Classify this cell by malaria status.
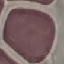

Uninfected.

stain = Giemsa
image type = automatically extracted cell patch, resized to 64 × 64 pixels
capture = smartphone through the microscope eyepiece
preparation = thin smear